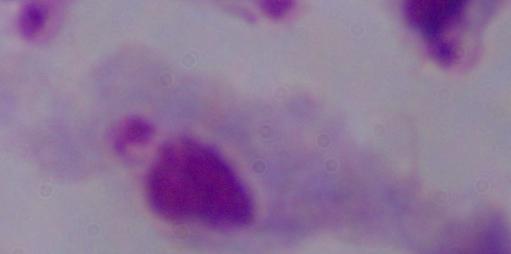

magnification = 1000x
identification = trichomonad
modality = micrograph